Locate and identify every blood parasite.
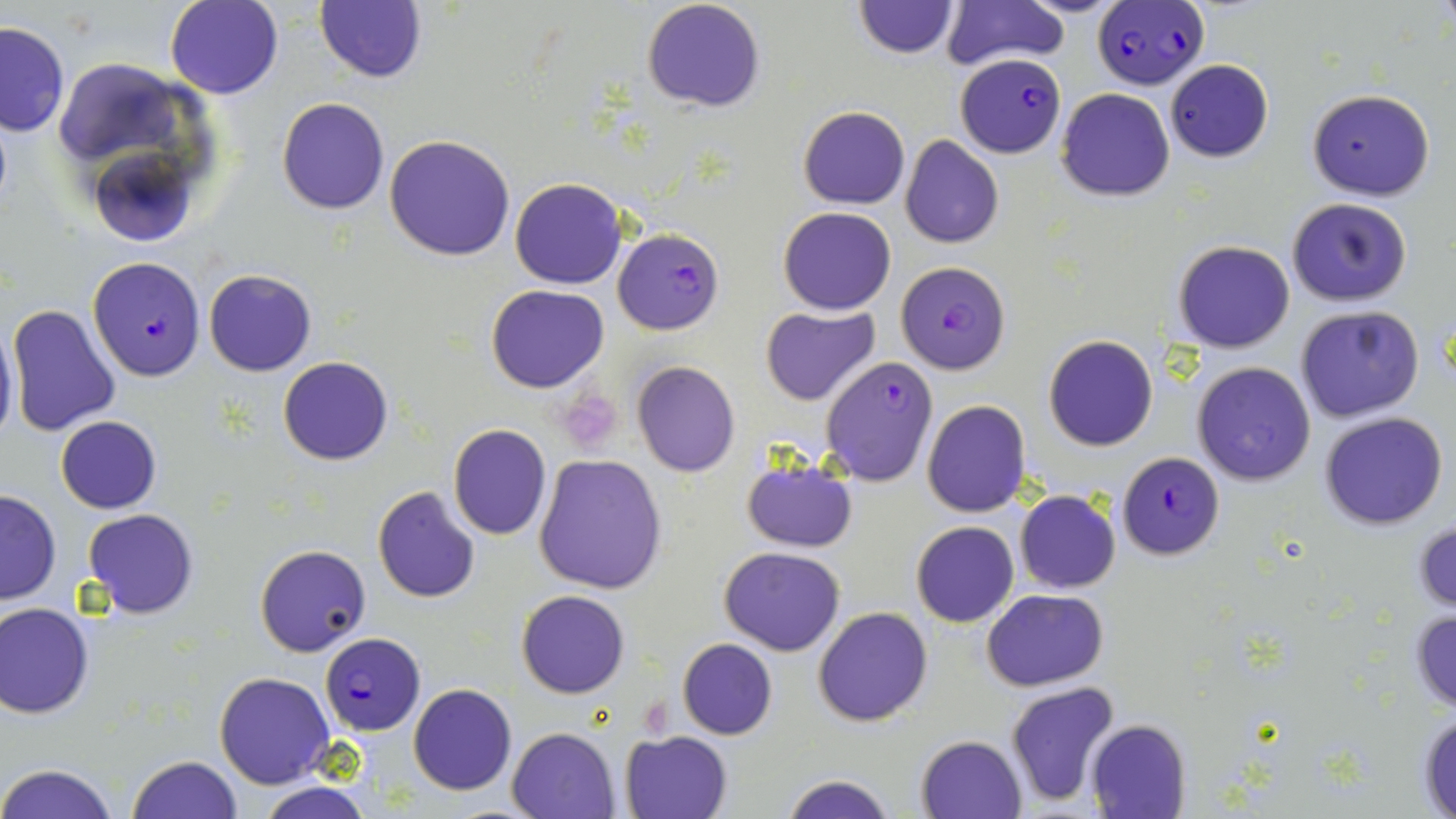

Approximate bounding boxes as named x1/y1/x2/y2 corners in pixels.
Plasmodium falciparum-infected red blood cells: (x1=1092, y1=1, x2=1209, y2=91), (x1=951, y1=58, x2=1065, y2=154), (x1=613, y1=228, x2=724, y2=335), (x1=87, y1=256, x2=207, y2=381), (x1=895, y1=261, x2=1012, y2=376), (x1=820, y1=359, x2=936, y2=487), (x1=1117, y1=452, x2=1224, y2=560), (x1=320, y1=634, x2=426, y2=735).
No Plasmodium ovale, Plasmodium malariae, Plasmodium vivax, Babesia divergens, or Trypanosoma brucei observed.

slide-level diagnosis = Plasmodium falciparum
magnification = 1000x
image size = 1456×819 pixels
preparation = thin blood smear
stain = May-Grünwald-Giemsa
field of view = single
platelet locations = approximate bounding boxes as named x1/y1/x2/y2 corners in pixels: (x1=564, y1=392, x2=621, y2=443), (x1=638, y1=699, x2=673, y2=739)
modality = optical microscopy
uninfected red blood cell locations = approximate bounding boxes as named x1/y1/x2/y2 corners in pixels: (x1=165, y1=0, x2=284, y2=100), (x1=642, y1=0, x2=766, y2=114), (x1=854, y1=0, x2=960, y2=58), (x1=942, y1=1, x2=1067, y2=72), (x1=314, y1=2, x2=427, y2=83), (x1=0, y1=21, x2=70, y2=136), (x1=1164, y1=59, x2=1274, y2=162), (x1=56, y1=64, x2=186, y2=156), (x1=1055, y1=87, x2=1176, y2=202), (x1=1305, y1=88, x2=1435, y2=201), (x1=276, y1=97, x2=390, y2=213), (x1=799, y1=106, x2=909, y2=209), (x1=383, y1=134, x2=515, y2=261), (x1=900, y1=136, x2=1004, y2=250), (x1=96, y1=159, x2=190, y2=246), (x1=510, y1=177, x2=627, y2=288), (x1=1288, y1=197, x2=1413, y2=307), (x1=777, y1=207, x2=896, y2=314), (x1=1173, y1=241, x2=1294, y2=352), (x1=204, y1=269, x2=316, y2=376), (x1=486, y1=284, x2=609, y2=394), (x1=8, y1=303, x2=121, y2=436), (x1=760, y1=305, x2=881, y2=405), (x1=1295, y1=306, x2=1424, y2=424), (x1=0, y1=322, x2=19, y2=450), (x1=1043, y1=335, x2=1158, y2=451), (x1=279, y1=356, x2=393, y2=465), (x1=1191, y1=361, x2=1317, y2=486), (x1=632, y1=362, x2=741, y2=477), (x1=922, y1=399, x2=1032, y2=518), (x1=1319, y1=411, x2=1448, y2=530), (x1=56, y1=415, x2=161, y2=513), (x1=447, y1=424, x2=552, y2=542), (x1=534, y1=454, x2=667, y2=594), (x1=739, y1=460, x2=857, y2=552), (x1=371, y1=485, x2=481, y2=604), (x1=0, y1=487, x2=61, y2=606), (x1=1015, y1=490, x2=1121, y2=594), (x1=83, y1=509, x2=198, y2=619), (x1=1414, y1=516, x2=1456, y2=615), (x1=911, y1=520, x2=1019, y2=628), (x1=255, y1=544, x2=371, y2=657), (x1=719, y1=546, x2=846, y2=655), (x1=981, y1=589, x2=1108, y2=690), (x1=516, y1=590, x2=630, y2=699), (x1=0, y1=602, x2=93, y2=719), (x1=812, y1=605, x2=934, y2=726), (x1=1409, y1=607, x2=1456, y2=712), (x1=678, y1=639, x2=777, y2=739), (x1=214, y1=673, x2=336, y2=790), (x1=1004, y1=683, x2=1121, y2=810), (x1=408, y1=684, x2=517, y2=796), (x1=1416, y1=706, x2=1456, y2=815), (x1=1087, y1=719, x2=1192, y2=819), (x1=507, y1=726, x2=620, y2=819), (x1=620, y1=730, x2=732, y2=818), (x1=916, y1=735, x2=1026, y2=819), (x1=127, y1=755, x2=243, y2=819), (x1=0, y1=762, x2=121, y2=819), (x1=780, y1=775, x2=898, y2=819), (x1=254, y1=783, x2=377, y2=819)